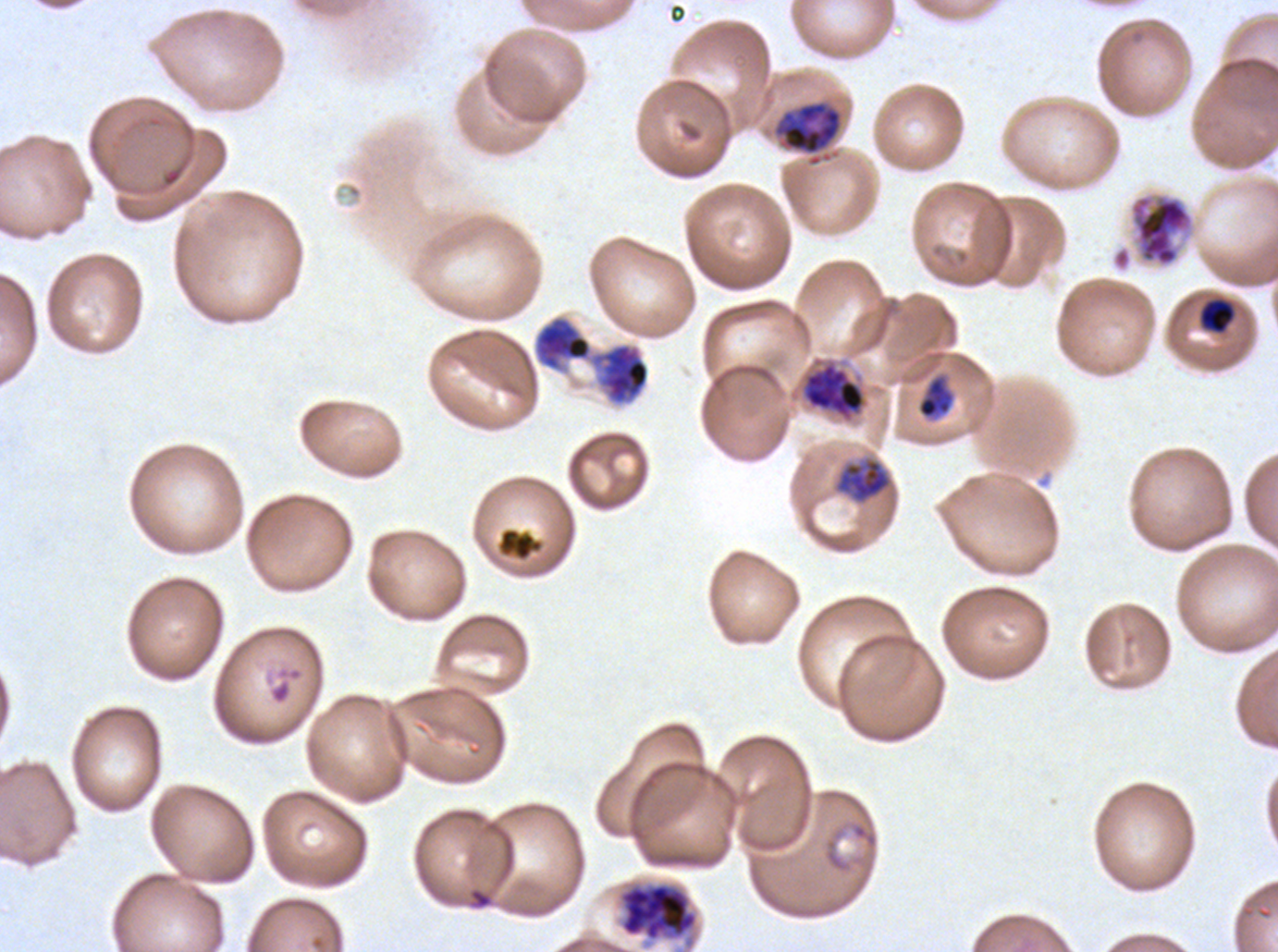 Approximate bounding boxes as [x1, y1, x2, y2] in pixels. Late trophozoite locations: [777, 101, 842, 155], [533, 314, 650, 405]. Late-ring/early-trophozoite locations: [1199, 299, 1235, 333], [916, 374, 955, 420]. Mid trophozoite locations: [803, 362, 866, 418], [835, 458, 891, 503]. Object labeled both mid trophozoite and early schizont by the source: [618, 881, 699, 943]. Late schizont locations: [1128, 191, 1196, 269], [533, 314, 650, 405] (two touching objects share this one region). Debris locations: [496, 527, 545, 562]. Plasmodium falciparum cultured ex vivo for 24 to 48 hours, from a patient in The Gambia. Giemsa-stained preparation. Image is 1278×952 pixels. A sub-image separated from a larger composite. Thin blood smear. Life-cycle stages observed: late-ring/early-trophozoite, mid trophozoite, late trophozoite, late schizont.